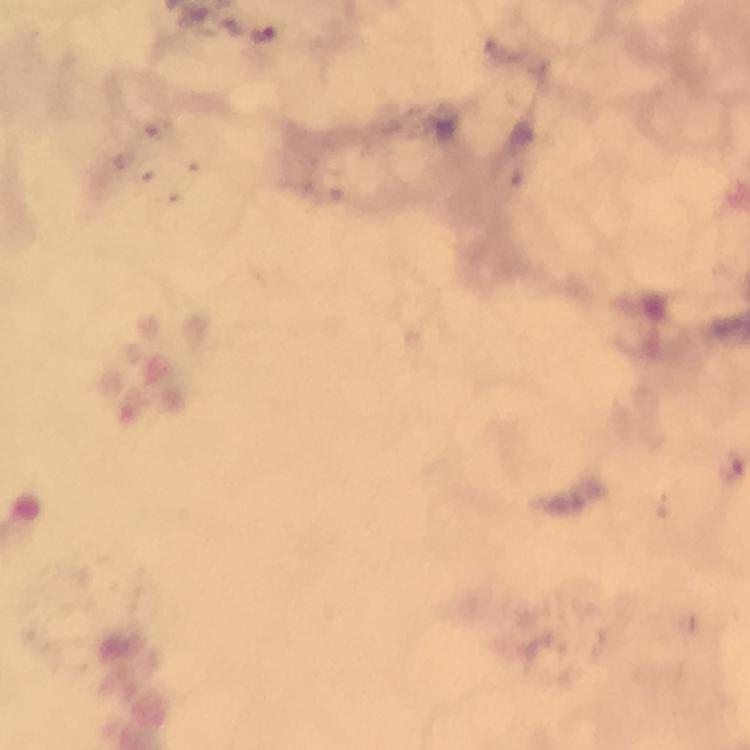

Approximate centers as [x, y] in pixels. Malaria parasite locations: [263, 34]. 100x magnification. Thick smear. Image is 750×750 pixels. Giemsa-stained preparation. From a diagnostic examination for malaria. Photographed with a smartphone mounted on the microscope. Cropped region of a single field of view. Immersion oil was used.